Classify this cell by malaria status.
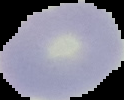

Uninfected.

image_type: segmented cell region on a black background
preparation: thin blood film
image_size: 124×100 pixels